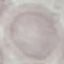

Summary:
  - Malaria status: uninfected
  - Preparation: thin blood film
  - Image type: automatically extracted cell patch, resized to 64 × 64 pixels
  - Stain: Giemsa
  - Capture: smartphone through the microscope eyepiece